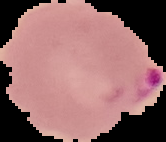
Summary:
  - Preparation: thin blood film
  - Malaria status: parasitized
  - Image size: 166×142 pixels
  - Image type: segmented cell region with the area outside set to black